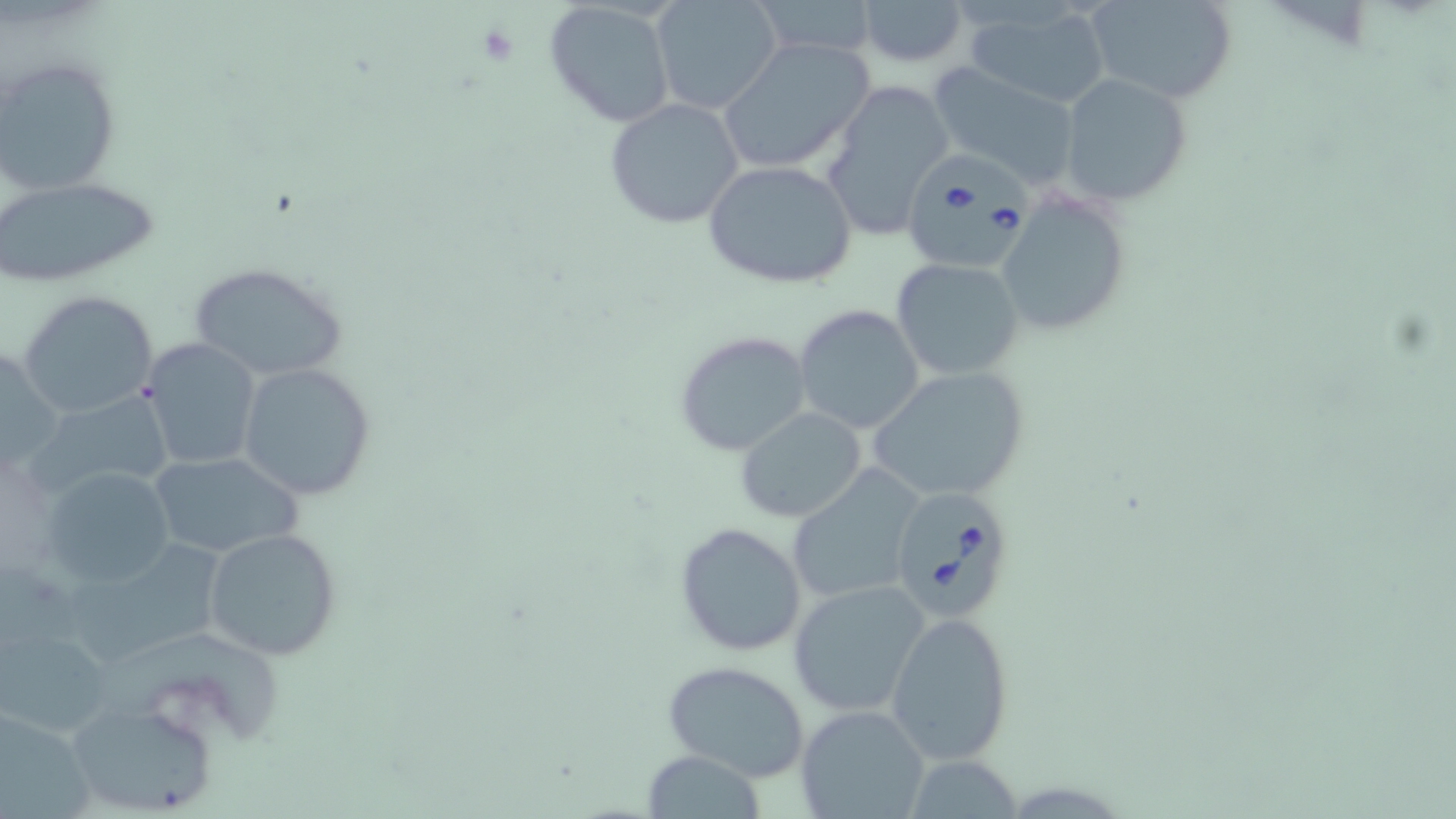
Approximate bounding boxes as named x1/y1/x2/y2 corners in pixels. Uninfected red blood cell locations: (x1=650, y1=0, x2=783, y2=115), (x1=749, y1=0, x2=879, y2=57), (x1=856, y1=0, x2=968, y2=67), (x1=1083, y1=0, x2=1239, y2=105), (x1=542, y1=2, x2=677, y2=128), (x1=967, y1=4, x2=1111, y2=110), (x1=719, y1=37, x2=875, y2=175), (x1=1, y1=56, x2=122, y2=197), (x1=927, y1=61, x2=1082, y2=185), (x1=1056, y1=73, x2=1193, y2=209), (x1=824, y1=81, x2=957, y2=238), (x1=605, y1=97, x2=745, y2=229), (x1=702, y1=160, x2=858, y2=289), (x1=1, y1=176, x2=158, y2=288), (x1=993, y1=188, x2=1134, y2=338), (x1=890, y1=257, x2=1026, y2=382), (x1=190, y1=262, x2=346, y2=381), (x1=19, y1=290, x2=159, y2=419), (x1=793, y1=305, x2=925, y2=435), (x1=674, y1=329, x2=812, y2=457), (x1=140, y1=337, x2=264, y2=471), (x1=237, y1=362, x2=376, y2=499), (x1=866, y1=367, x2=1030, y2=501), (x1=28, y1=388, x2=178, y2=503), (x1=735, y1=407, x2=867, y2=524), (x1=147, y1=451, x2=304, y2=562), (x1=41, y1=465, x2=178, y2=587), (x1=789, y1=472, x2=922, y2=606), (x1=675, y1=521, x2=808, y2=656), (x1=66, y1=527, x2=248, y2=662), (x1=202, y1=527, x2=342, y2=661), (x1=786, y1=578, x2=931, y2=716), (x1=886, y1=610, x2=1017, y2=765), (x1=108, y1=633, x2=297, y2=746), (x1=3, y1=637, x2=104, y2=735), (x1=661, y1=660, x2=812, y2=784), (x1=796, y1=703, x2=930, y2=819), (x1=72, y1=704, x2=214, y2=811), (x1=0, y1=708, x2=108, y2=819), (x1=640, y1=751, x2=766, y2=816), (x1=906, y1=753, x2=1023, y2=818). Platelet locations: (x1=474, y1=20, x2=521, y2=67). Babesia divergens-infected red blood cell locations: (x1=904, y1=146, x2=1040, y2=268), (x1=887, y1=486, x2=1019, y2=624). Slide-level diagnosis: Babesia divergens. 1000x magnification. Optical microscopy. Thin blood film. One field of a larger specimen. Image is 1456×819 pixels. May-Grünwald-Giemsa stain.